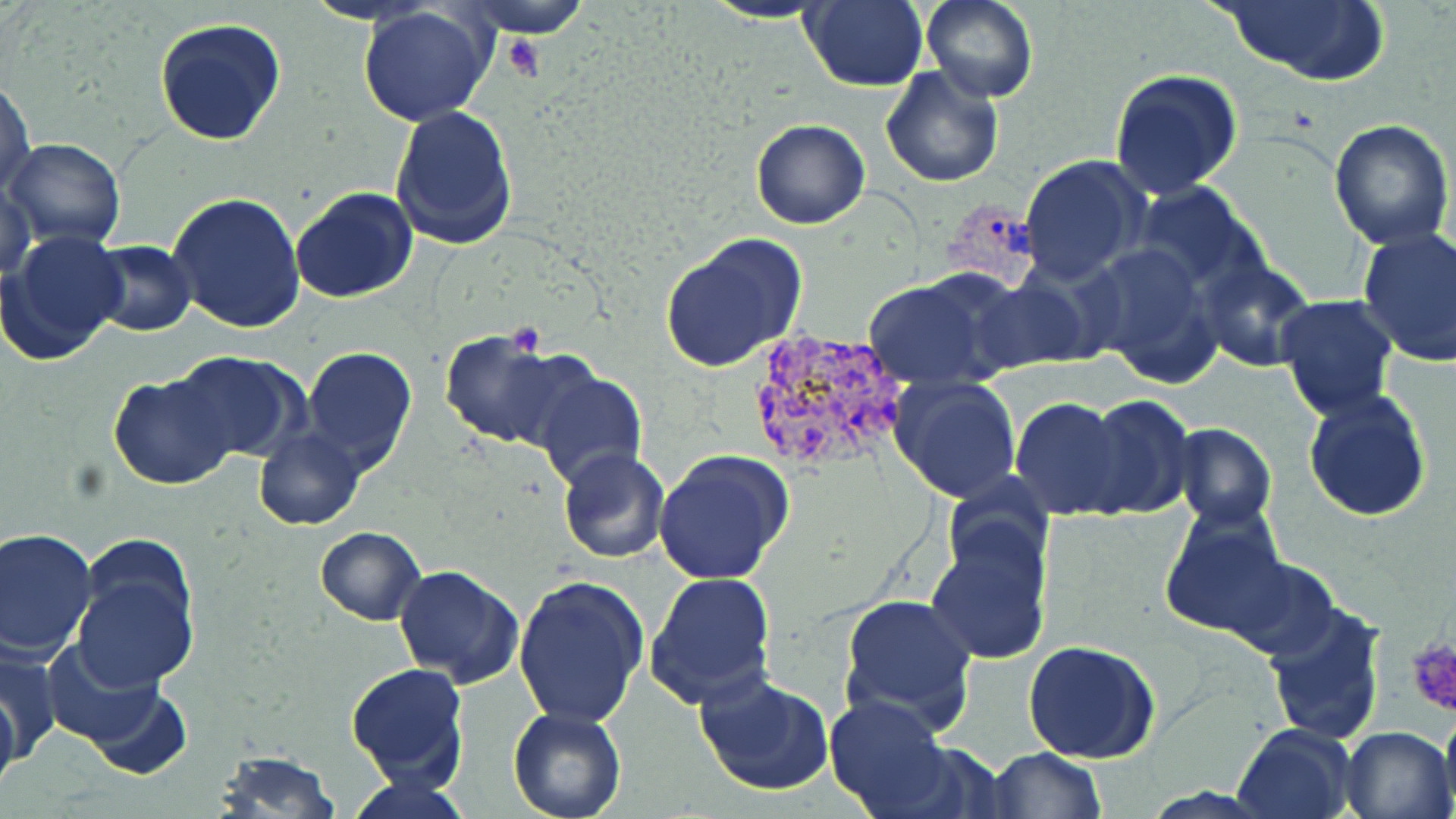

{
  "slide_level_diagnosis": "Plasmodium vivax",
  "magnification": "1000x",
  "platelet_locations": "approximate bounding boxes as [x1, y1, x2, y2] in pixels: [503, 34, 548, 82], [504, 322, 546, 358], [1405, 633, 1456, 715]",
  "preparation": "thin blood smear",
  "plasmodium_vivax_infected_red_blood_cell_locations": "approximate bounding boxes as [x1, y1, x2, y2] in pixels: [939, 196, 1044, 292], [745, 325, 910, 478]",
  "field_of_view": "one of a larger specimen",
  "stain": "May-Grünwald-Giemsa",
  "image_size": "1456×819 pixels",
  "modality": "light microscopy",
  "uninfected_red_blood_cell_locations": "approximate bounding boxes as [x1, y1, x2, y2] in pixels: [460, 0, 593, 40], [921, 0, 1037, 103], [1216, 0, 1390, 87], [700, 1, 835, 25], [801, 1, 929, 92], [354, 7, 496, 127], [154, 17, 287, 145], [879, 66, 1004, 188], [1110, 67, 1243, 197], [1, 78, 36, 199], [389, 106, 519, 251], [751, 118, 870, 229], [1328, 118, 1455, 250], [4, 139, 125, 249], [1017, 154, 1153, 287], [1, 180, 38, 280], [1134, 182, 1267, 299], [290, 187, 419, 303], [166, 191, 306, 333], [1356, 228, 1456, 367], [4, 229, 128, 367], [659, 232, 809, 374], [87, 240, 195, 337], [1083, 241, 1225, 389], [1201, 258, 1314, 373], [977, 267, 1100, 370], [862, 273, 1012, 390], [1274, 295, 1401, 422], [438, 329, 574, 450], [300, 345, 416, 475], [167, 351, 309, 463], [524, 364, 648, 492], [108, 372, 238, 490], [889, 374, 1023, 503], [1303, 388, 1434, 521], [1080, 394, 1195, 522], [1010, 396, 1132, 521], [1171, 424, 1277, 529], [254, 430, 366, 531], [653, 447, 794, 585], [557, 449, 669, 564], [1159, 505, 1289, 643], [925, 521, 1052, 667], [315, 527, 426, 625], [0, 528, 98, 658], [70, 552, 201, 693], [1221, 552, 1340, 660], [393, 565, 524, 688], [645, 571, 777, 711], [513, 574, 648, 729], [839, 594, 979, 732], [1260, 601, 1389, 745], [1022, 640, 1160, 764], [44, 641, 181, 766], [0, 642, 62, 762], [346, 663, 470, 789], [695, 671, 834, 797], [0, 685, 19, 799], [83, 687, 193, 779], [824, 692, 957, 818], [1439, 699, 1456, 815], [508, 708, 628, 819], [1231, 721, 1357, 818], [1338, 725, 1455, 819], [982, 747, 1107, 818], [211, 751, 340, 818], [348, 773, 472, 819]"
}